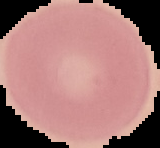

{
  "preparation": "thin blood film",
  "image_size": "160×148 pixels",
  "image_type": "segmented cell region on a black background",
  "result": "negative for malaria parasites"
}